Locate every Plasmodium vivax-infected red blood cell.
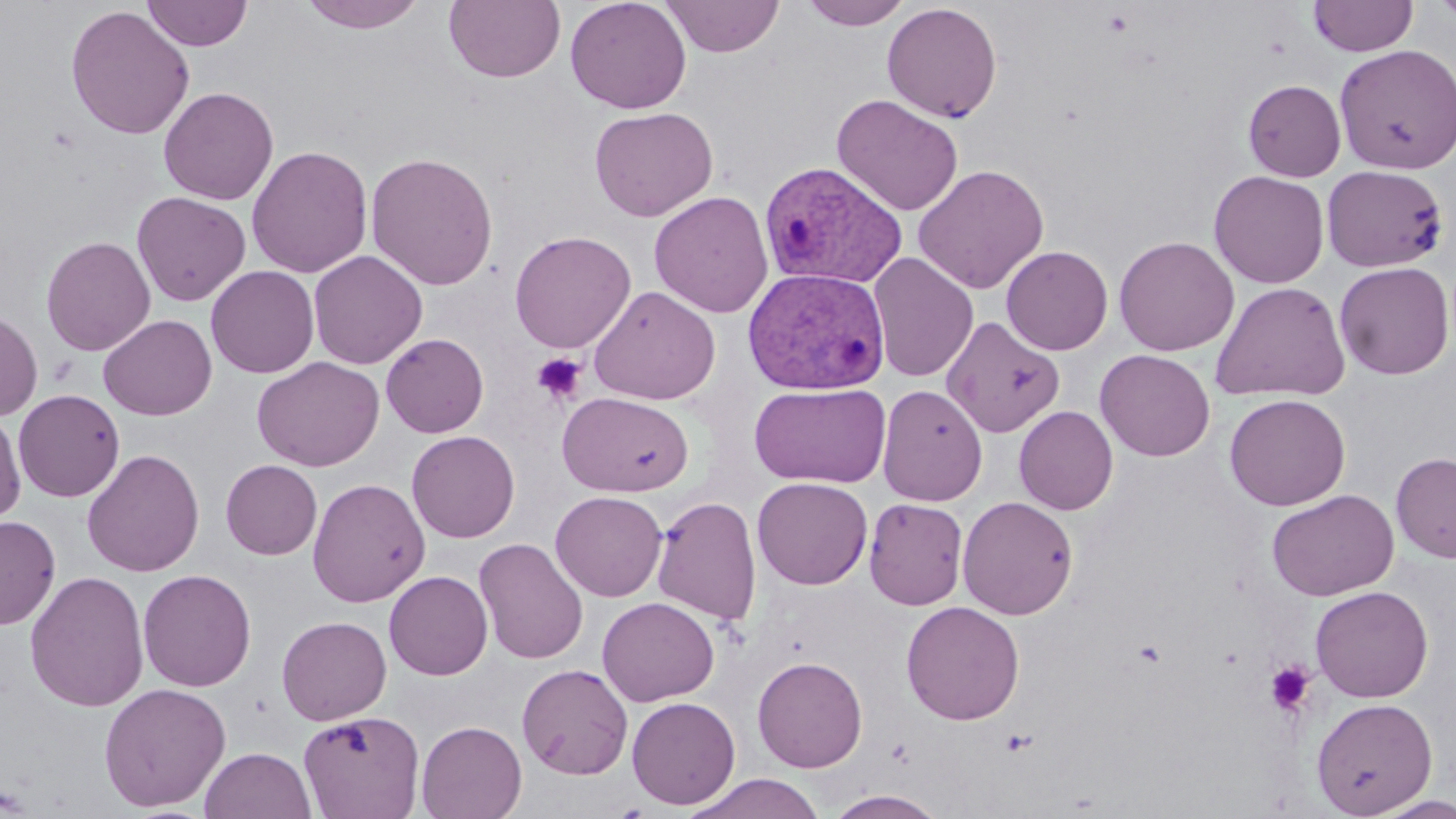
Approximate bounding boxes as [x1, y1, x2, y2] in pixels.
Plasmodium vivax-infected red blood cells: [759, 161, 908, 291], [742, 266, 890, 395].

Summary:
  - Uninfected red blood cell locations: [142, 0, 253, 51], [297, 0, 429, 34], [443, 0, 566, 84], [565, 0, 692, 114], [660, 0, 785, 58], [799, 0, 912, 30], [1308, 0, 1417, 57], [1432, 0, 1456, 31], [882, 3, 1003, 123], [65, 5, 195, 140], [1334, 44, 1456, 173], [1243, 79, 1346, 182], [159, 86, 279, 205], [832, 94, 964, 216], [589, 106, 718, 221], [246, 144, 373, 278], [365, 151, 499, 291], [912, 163, 1050, 294], [1321, 164, 1448, 273], [1208, 170, 1330, 289], [649, 190, 773, 318], [131, 191, 251, 306], [509, 230, 636, 353], [40, 235, 156, 356], [1114, 235, 1239, 356], [1001, 245, 1114, 355], [309, 250, 428, 369], [867, 252, 979, 382], [1333, 261, 1454, 380], [205, 265, 320, 378], [1210, 281, 1351, 402], [588, 285, 721, 405], [0, 309, 42, 421], [98, 315, 217, 420], [941, 316, 1065, 437], [381, 333, 489, 438], [1094, 349, 1216, 461], [252, 356, 385, 471], [749, 382, 891, 488], [877, 384, 988, 505], [13, 389, 125, 502], [557, 391, 693, 496], [1224, 393, 1351, 511], [1014, 406, 1118, 515], [0, 409, 26, 525], [406, 430, 520, 542], [82, 448, 204, 577], [1391, 451, 1456, 563], [221, 460, 322, 559], [752, 477, 873, 589], [307, 478, 430, 607], [1266, 489, 1399, 601], [550, 491, 667, 601], [957, 495, 1079, 620], [652, 496, 762, 626], [864, 498, 969, 610], [0, 515, 61, 630], [474, 538, 589, 665], [138, 569, 257, 692], [24, 570, 149, 713], [384, 570, 493, 680], [1310, 585, 1433, 702], [597, 597, 720, 707], [901, 600, 1025, 725], [276, 615, 392, 725], [752, 655, 868, 772], [517, 663, 633, 779], [98, 682, 231, 811], [627, 696, 741, 810], [1311, 697, 1438, 817], [298, 710, 425, 819], [416, 720, 527, 819], [199, 746, 317, 819], [684, 772, 827, 819], [825, 789, 949, 818], [1369, 794, 1456, 818]
  - Platelet locations: [532, 352, 587, 406], [1264, 661, 1315, 716]
  - Slide-level diagnosis: Plasmodium vivax
  - Modality: optical microscopy
  - Stain: May-Grünwald-Giemsa
  - Field of view: single
  - Preparation: thin blood smear
  - Image size: 1456×819 pixels
  - Magnification: 1000x